Identify the parasite.
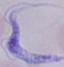

A trypanosome.

Photomicrograph. Captured at 1000x magnification.